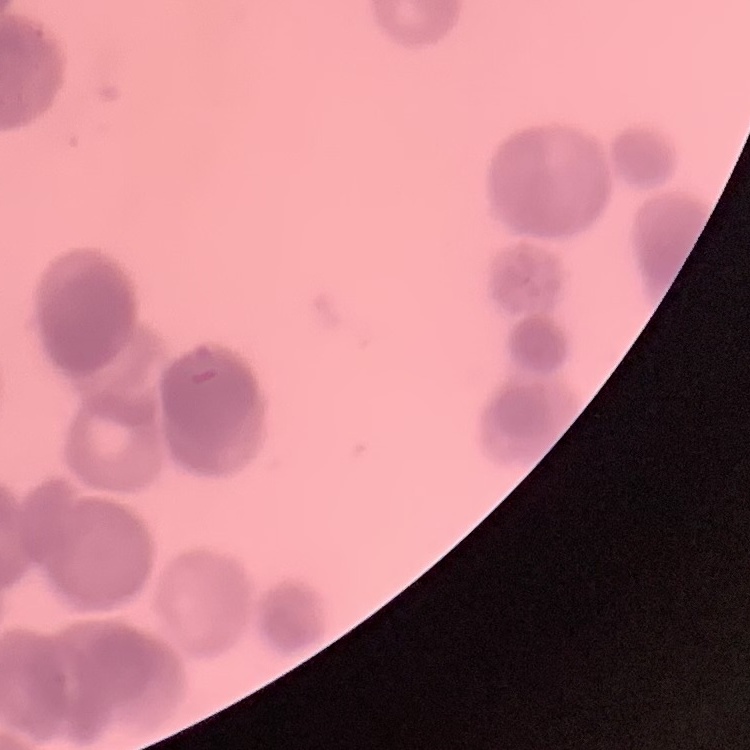
{
  "red_blood_cell_morphology": "rouleaux formation",
  "preparation": "thin blood film",
  "stain": "Field's or Giemsa",
  "image_type": "square crop of a larger photomicrograph"
}